Assess this cell for malaria.
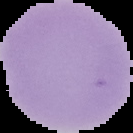
Uninfected.

Summary:
  - Image size: 133×133 pixels
  - Image type: segmented cell region on a black background
  - Preparation: thin blood smear